Evaluate for Plasmodium parasites.
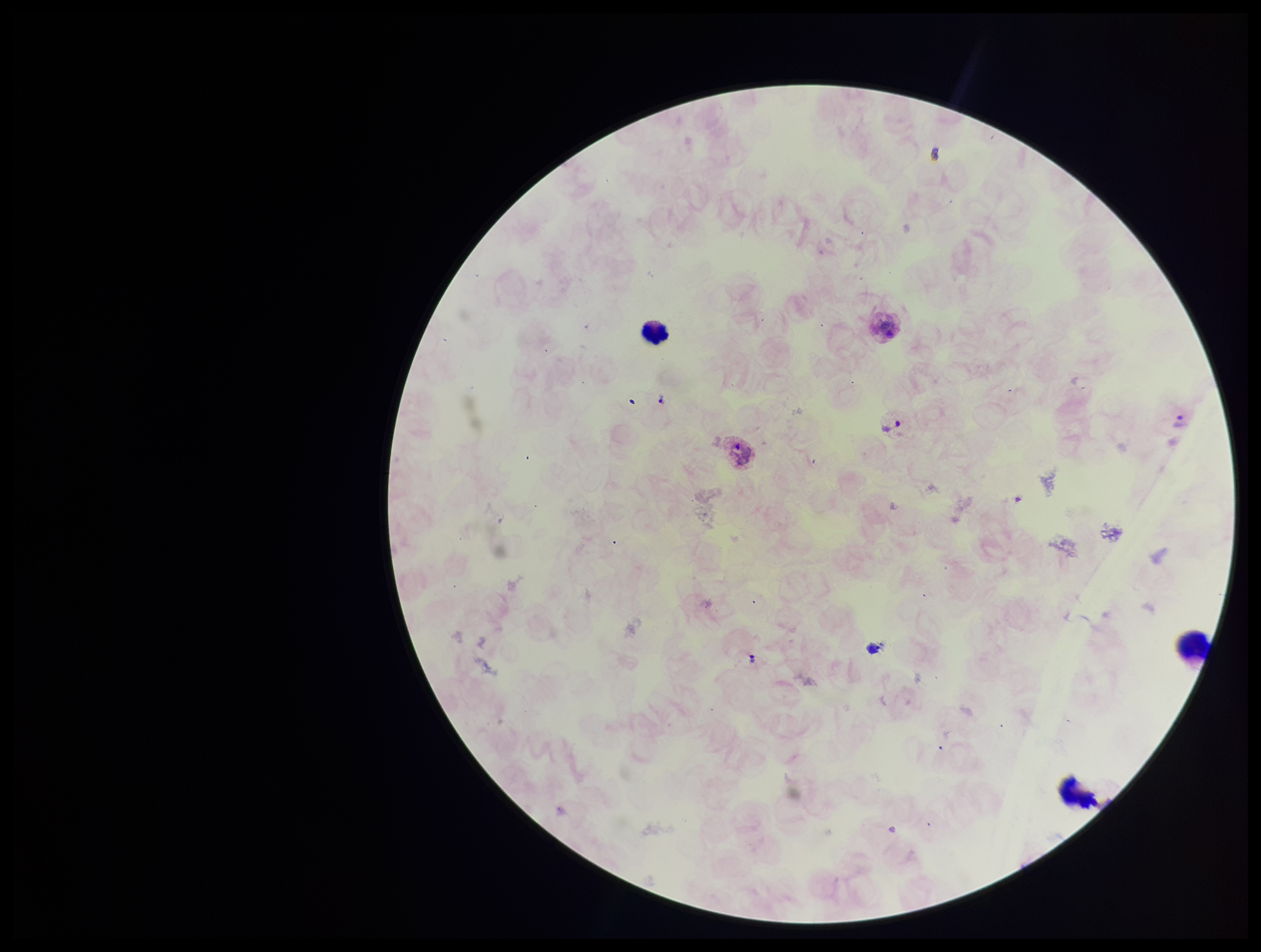
Seen.

parasite_count: 3
species_reported_for_this_patient: Plasmodium vivax
preparation: thick
patient_malaria_status: positive
capture: smartphone photograph through the microscope eyepiece
field_of_view: one from this slide
stain: Giemsa
image_size: 1261×952 pixels
leukocyte_count: 3